State which parasite is depicted.
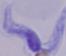
This is a trypanosome.

Micrograph. 1000x magnification.